Assess this cell for malaria.
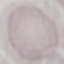
It is uninfected.

{
  "capture": "smartphone camera at the microscope eyepiece",
  "preparation": "thin smear",
  "image_type": "cell patch, automatically extracted from a larger field of view and resized to 64 × 64 pixels",
  "stain": "Giemsa"
}